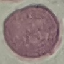

result = no malaria parasites seen
stain = Giemsa
image type = cell patch, automatically extracted from a larger field of view and resized to 64 × 64 pixels
preparation = thin blood film
capture = smartphone camera at the microscope eyepiece